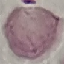

Result: no malaria parasites seen. Thin smear of blood. Giemsa stain. Acquired by smartphone through the microscope eyepiece. Automatically extracted cell patch, resized to 64 × 64 pixels.